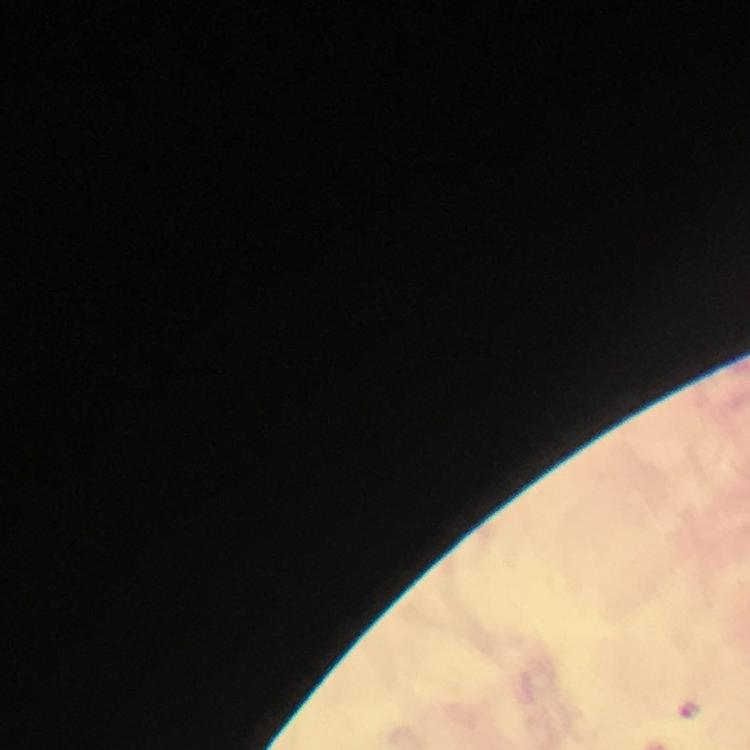
stain: Giemsa
context: from a diagnostic examination for malaria
image_size: 750×750 pixels
preparation: thick blood film
immersion_oil: used
plasmodium_parasite_locations: 'approximate centers as [x, y] in pixels: [692, 709]'
cropped_from: one field of view
magnification: 100x
capture: smartphone camera through the microscope